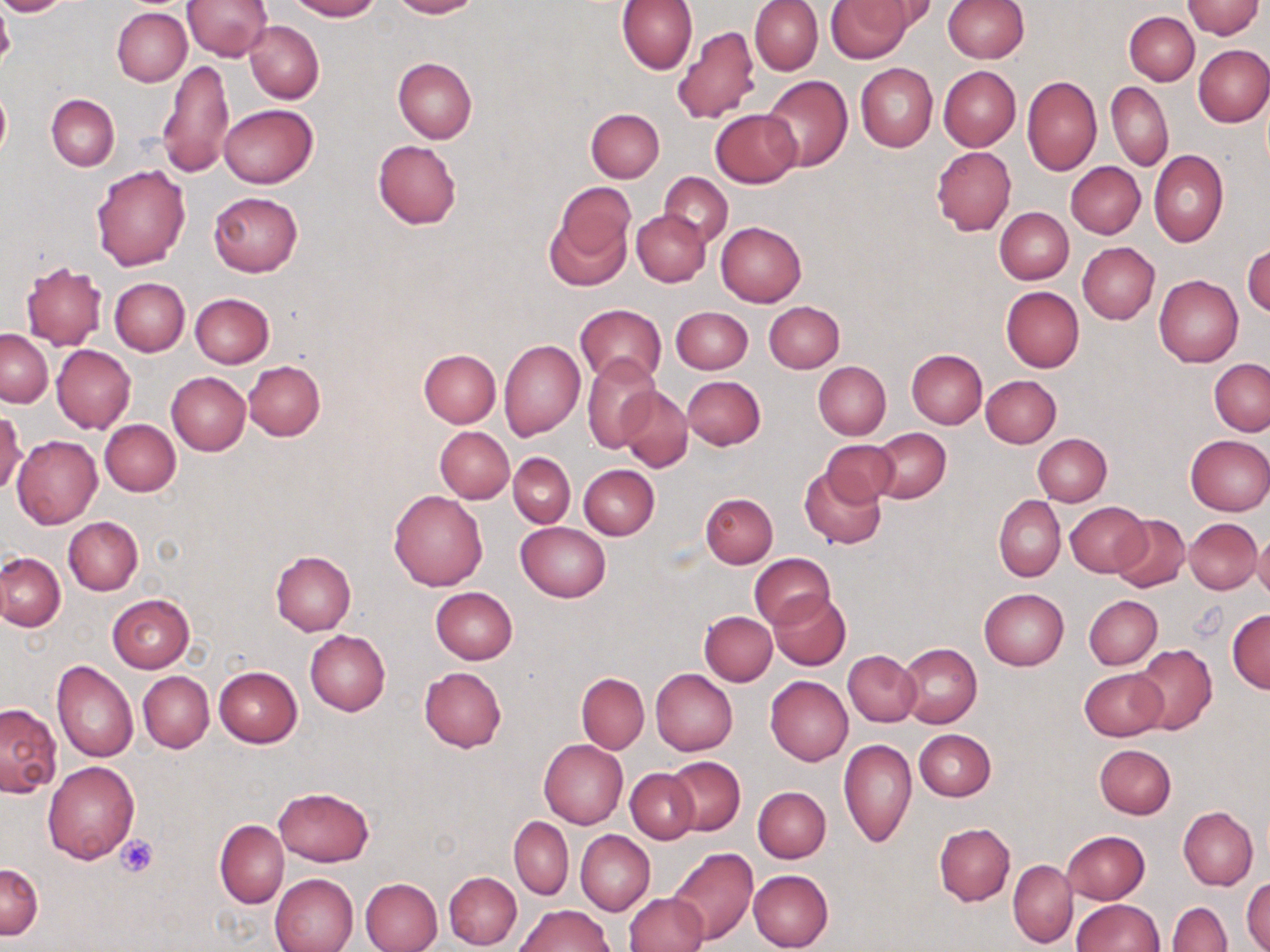
slide_level_diagnosis: no evidence of blood parasites
uninfected_red_blood_cell_locations: 'approximate bounding boxes as named x1/y1/x2/y2 corners in pixels: (x1=0, y1=0, x2=77, y2=16), (x1=182, y1=0, x2=273, y2=61), (x1=288, y1=0, x2=381, y2=20), (x1=389, y1=0, x2=481, y2=18), (x1=750, y1=0, x2=823, y2=76), (x1=826, y1=0, x2=912, y2=62), (x1=942, y1=0, x2=1028, y2=63), (x1=1183, y1=0, x2=1263, y2=39), (x1=616, y1=1, x2=698, y2=74), (x1=854, y1=1, x2=939, y2=42), (x1=112, y1=7, x2=192, y2=86), (x1=1124, y1=12, x2=1200, y2=85), (x1=244, y1=20, x2=323, y2=104), (x1=672, y1=25, x2=761, y2=126), (x1=1193, y1=44, x2=1270, y2=126), (x1=393, y1=57, x2=476, y2=144), (x1=158, y1=60, x2=234, y2=177), (x1=856, y1=63, x2=938, y2=152), (x1=939, y1=66, x2=1019, y2=150), (x1=761, y1=75, x2=852, y2=170), (x1=1022, y1=76, x2=1101, y2=175), (x1=1106, y1=82, x2=1173, y2=171), (x1=0, y1=86, x2=11, y2=163), (x1=47, y1=94, x2=119, y2=171), (x1=218, y1=103, x2=317, y2=188), (x1=586, y1=109, x2=664, y2=182), (x1=710, y1=109, x2=802, y2=187), (x1=372, y1=140, x2=462, y2=229), (x1=931, y1=146, x2=1016, y2=235), (x1=1149, y1=150, x2=1227, y2=247), (x1=1067, y1=161, x2=1145, y2=239), (x1=90, y1=165, x2=190, y2=270), (x1=659, y1=172, x2=734, y2=245), (x1=552, y1=180, x2=635, y2=271), (x1=209, y1=191, x2=301, y2=276), (x1=995, y1=207, x2=1074, y2=284), (x1=633, y1=211, x2=710, y2=285), (x1=715, y1=222, x2=806, y2=307), (x1=1077, y1=242, x2=1159, y2=323), (x1=1243, y1=243, x2=1270, y2=318), (x1=21, y1=262, x2=107, y2=349), (x1=1154, y1=274, x2=1244, y2=367), (x1=109, y1=277, x2=189, y2=356), (x1=1001, y1=286, x2=1084, y2=372), (x1=190, y1=293, x2=274, y2=368), (x1=764, y1=301, x2=845, y2=373), (x1=576, y1=304, x2=666, y2=386), (x1=670, y1=306, x2=753, y2=374), (x1=0, y1=330, x2=52, y2=407), (x1=499, y1=338, x2=585, y2=440), (x1=52, y1=344, x2=136, y2=434), (x1=418, y1=349, x2=501, y2=428), (x1=906, y1=349, x2=987, y2=428), (x1=582, y1=355, x2=661, y2=452), (x1=1210, y1=359, x2=1270, y2=436), (x1=244, y1=361, x2=325, y2=440), (x1=814, y1=361, x2=890, y2=439), (x1=167, y1=372, x2=250, y2=454), (x1=981, y1=375, x2=1060, y2=446), (x1=682, y1=376, x2=766, y2=449), (x1=617, y1=387, x2=693, y2=472), (x1=0, y1=410, x2=27, y2=496), (x1=100, y1=419, x2=180, y2=496), (x1=435, y1=427, x2=514, y2=503), (x1=871, y1=427, x2=950, y2=502), (x1=1032, y1=433, x2=1112, y2=506), (x1=13, y1=435, x2=102, y2=527), (x1=1185, y1=435, x2=1270, y2=515), (x1=822, y1=440, x2=900, y2=504), (x1=508, y1=452, x2=575, y2=528), (x1=509, y1=453, x2=585, y2=600), (x1=579, y1=464, x2=659, y2=539), (x1=800, y1=465, x2=886, y2=549), (x1=389, y1=490, x2=488, y2=591), (x1=701, y1=492, x2=778, y2=568), (x1=993, y1=496, x2=1065, y2=581), (x1=1064, y1=502, x2=1150, y2=577), (x1=1110, y1=514, x2=1190, y2=593), (x1=64, y1=516, x2=143, y2=596), (x1=1185, y1=518, x2=1261, y2=594), (x1=516, y1=521, x2=612, y2=602), (x1=1254, y1=531, x2=1270, y2=603), (x1=271, y1=551, x2=356, y2=635), (x1=0, y1=552, x2=65, y2=630), (x1=750, y1=553, x2=834, y2=629), (x1=430, y1=587, x2=517, y2=664), (x1=979, y1=588, x2=1069, y2=670), (x1=769, y1=591, x2=850, y2=670), (x1=107, y1=593, x2=194, y2=672), (x1=1084, y1=595, x2=1161, y2=669), (x1=1227, y1=609, x2=1270, y2=693), (x1=699, y1=611, x2=777, y2=686), (x1=306, y1=630, x2=390, y2=716), (x1=898, y1=643, x2=981, y2=729), (x1=1134, y1=645, x2=1216, y2=735), (x1=843, y1=650, x2=921, y2=727), (x1=51, y1=660, x2=138, y2=762), (x1=213, y1=666, x2=302, y2=747), (x1=419, y1=667, x2=507, y2=752), (x1=1080, y1=668, x2=1168, y2=741), (x1=651, y1=669, x2=738, y2=755), (x1=138, y1=671, x2=214, y2=753), (x1=576, y1=672, x2=650, y2=753), (x1=765, y1=676, x2=853, y2=765), (x1=0, y1=702, x2=62, y2=796), (x1=915, y1=729, x2=995, y2=801), (x1=838, y1=738, x2=917, y2=848), (x1=539, y1=740, x2=628, y2=829), (x1=1094, y1=744, x2=1176, y2=819), (x1=667, y1=756, x2=746, y2=835), (x1=43, y1=762, x2=139, y2=863), (x1=626, y1=768, x2=699, y2=844), (x1=274, y1=786, x2=373, y2=866), (x1=752, y1=786, x2=830, y2=863), (x1=1179, y1=807, x2=1257, y2=889), (x1=510, y1=817, x2=573, y2=900), (x1=215, y1=820, x2=288, y2=908), (x1=933, y1=822, x2=1015, y2=905), (x1=575, y1=830, x2=655, y2=915), (x1=1061, y1=830, x2=1149, y2=904), (x1=665, y1=847, x2=757, y2=946), (x1=0, y1=860, x2=42, y2=939), (x1=1007, y1=860, x2=1078, y2=948), (x1=749, y1=869, x2=833, y2=952), (x1=444, y1=871, x2=521, y2=948), (x1=269, y1=873, x2=359, y2=952), (x1=1243, y1=876, x2=1270, y2=952), (x1=361, y1=877, x2=443, y2=952), (x1=623, y1=893, x2=707, y2=952), (x1=1073, y1=899, x2=1163, y2=950), (x1=1168, y1=902, x2=1231, y2=952), (x1=516, y1=904, x2=614, y2=952)'
image_size: 1270×952 pixels
field_of_view: single
preparation: thin blood smear
modality: light microscopy
magnification: 1000x
stain: May-Grünwald-Giemsa
platelet_locations: 'approximate bounding boxes as named x1/y1/x2/y2 corners in pixels: (x1=0, y1=7, x2=16, y2=66), (x1=115, y1=833, x2=158, y2=876)'